Report the malaria status of this cell.
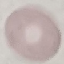

Uninfected.

{
  "stain": "Giemsa",
  "capture": "smartphone through the microscope eyepiece",
  "image_type": "cell patch, automatically extracted from a larger field of view and resized to 64 × 64 pixels",
  "preparation": "thin blood smear"
}